State which parasite is depicted.
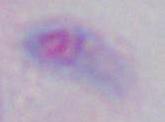

Toxoplasma gondii.

Summary:
  - Modality: micrograph
  - Magnification: 1000x